Report the malaria status of this cell.
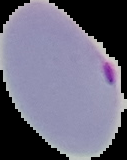
Parasitized.

preparation = thin blood smear
image type = segmented cell region on a black background
image size = 127×160 pixels